Classify this cell by malaria status.
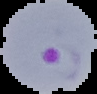
Parasitized.

image size = 97×94 pixels
preparation = thin blood smear
image type = segmented cell region with the area outside set to black